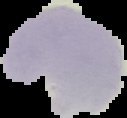
Result: no Plasmodium parasites seen. From a thin blood film. Image is 127×118 pixels. Segmented cell region on a black background.